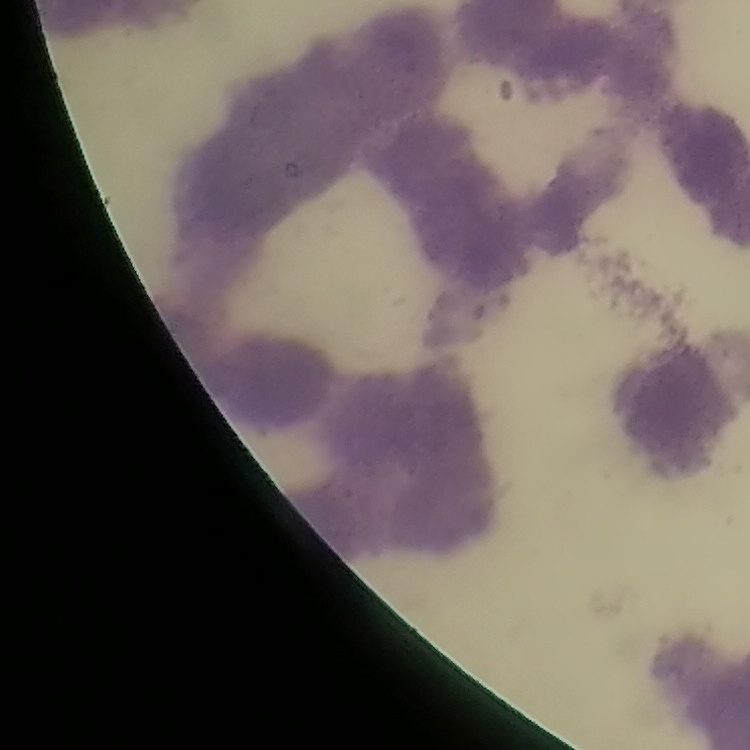

Summary:
  - Red blood cell morphology: rouleaux formation
  - Image type: one tile cut from a larger photomicrograph
  - Preparation: thin blood smear
  - Stain: Field's or Giemsa